Classify this cell by malaria status.
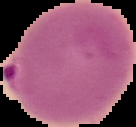
It is parasitized.

Segmented cell region on a black background. From a thin blood film. Image is 136×127 pixels.